Name the cell type shown.
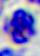

This is a leukocyte.

Summary:
  - Magnification: 400x
  - Modality: photomicrograph